Locate every Plasmodium parasite.
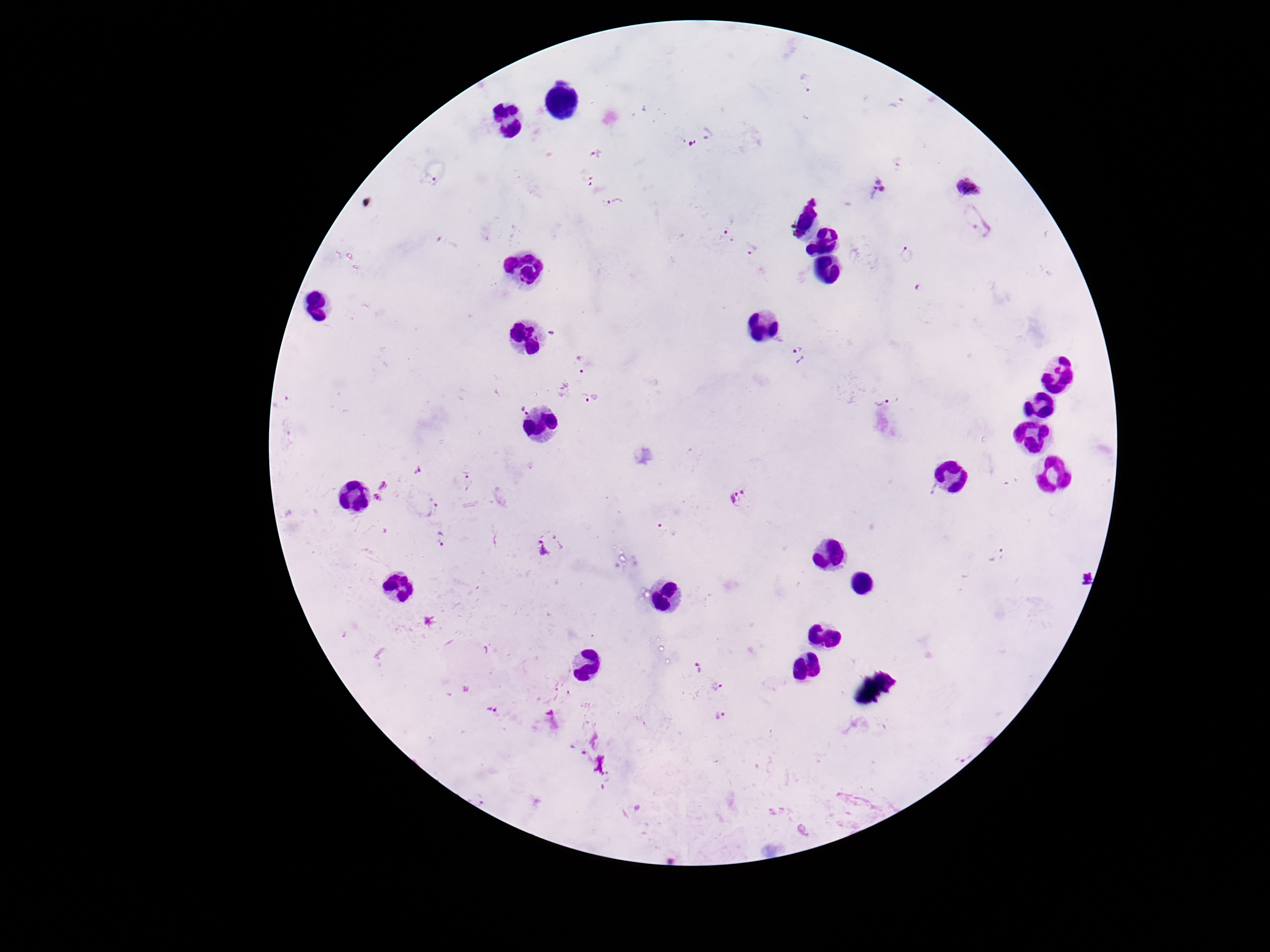

Approximate centers as [x, y] in pixels.
Plasmodium parasites: [806, 81], [708, 133], [680, 138], [694, 143], [597, 154], [899, 163], [433, 181], [587, 181], [880, 185], [968, 188], [614, 200], [979, 221], [726, 234], [449, 241], [753, 248], [907, 256], [922, 290], [552, 333], [798, 353], [580, 366], [586, 399], [888, 402], [523, 410], [418, 470], [1012, 481], [470, 482], [384, 486], [932, 488], [741, 494], [377, 501], [432, 506], [442, 539], [550, 547], [998, 554], [699, 669], [718, 685], [493, 711], [719, 717], [964, 756].

100x magnification. Image is 1270×952 pixels. Giemsa-stained preparation. Thick peripheral-blood smear. Smartphone photograph taken through the microscope eyepiece. One field from this slide. Patient malaria status: positive.